Assess this cell for malaria.
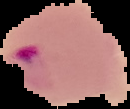

It is parasitized.

Image is 130×109 pixels. From a thin blood film. The area outside the segmented cell region is set to black.